Assess this cell for malaria.
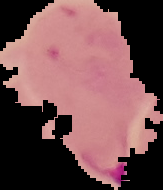
Parasitized.

image type = segmented cell region with the area outside set to black
image size = 163×190 pixels
preparation = thin blood film